Outline each blood parasite and name the species.
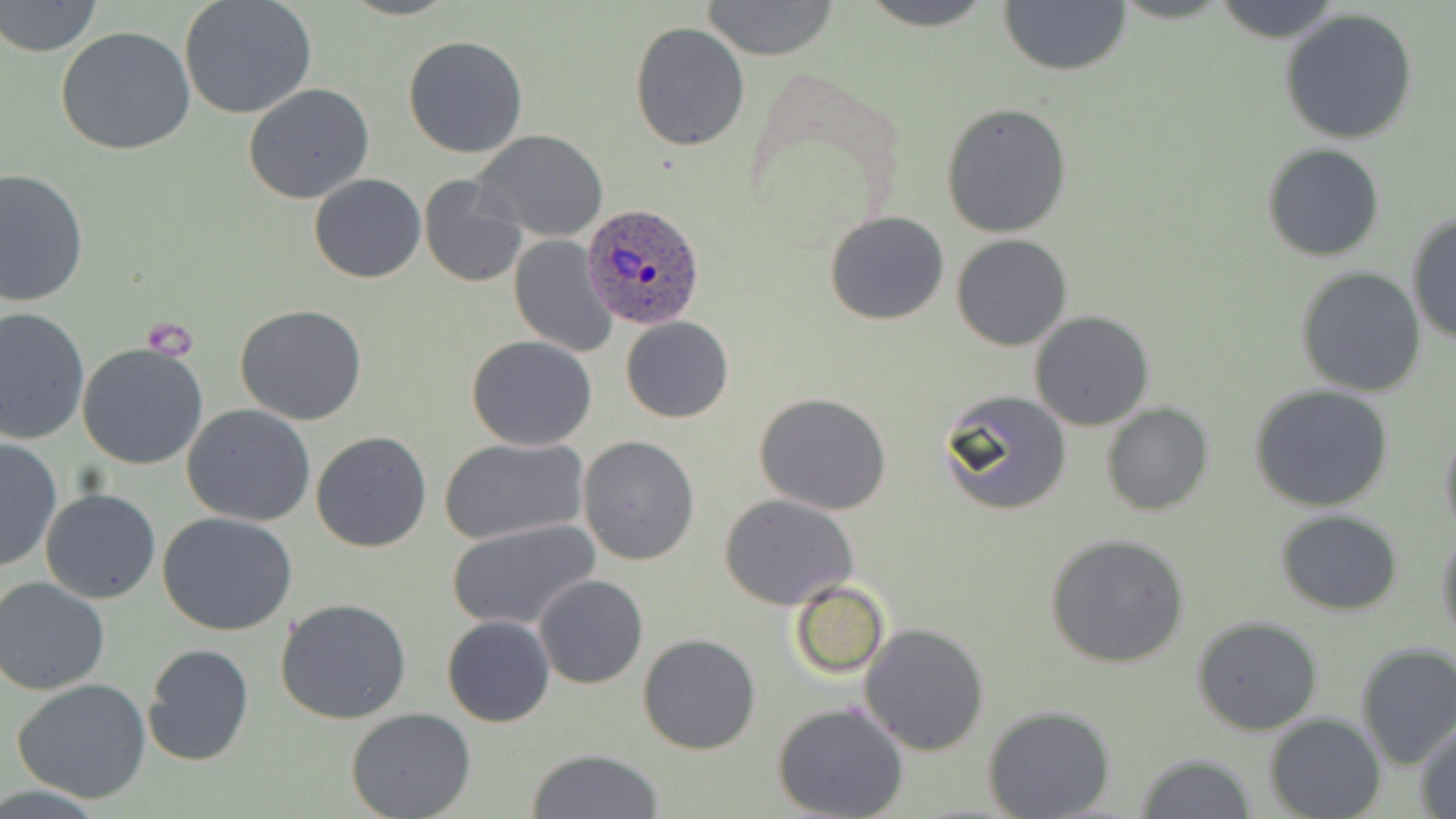
Approximate bounding boxes as (x1, y1, x2, y2) in pixels.
Plasmodium ovale-infected red blood cells: (581, 202, 705, 331).
No Plasmodium falciparum, Plasmodium malariae, Plasmodium vivax, Babesia divergens, or Trypanosoma brucei observed.

Summary:
  - Uninfected red blood cell locations: (178, 0, 317, 119), (702, 0, 840, 61), (859, 0, 996, 30), (998, 0, 1130, 77), (1210, 0, 1346, 45), (1, 1, 103, 57), (1278, 7, 1420, 145), (629, 21, 749, 151), (55, 25, 196, 156), (404, 34, 528, 157), (244, 84, 374, 205), (940, 102, 1072, 238), (472, 129, 608, 242), (1262, 143, 1384, 262), (0, 168, 89, 308), (310, 175, 426, 283), (418, 175, 527, 288), (825, 210, 948, 325), (1405, 211, 1455, 345), (951, 234, 1072, 351), (508, 235, 617, 357), (1296, 266, 1427, 397), (0, 305, 90, 445), (236, 305, 367, 425), (1028, 310, 1154, 432), (620, 316, 734, 424), (466, 335, 597, 451), (76, 342, 209, 470), (1250, 385, 1396, 513), (940, 388, 1073, 517), (755, 393, 892, 516), (1101, 402, 1214, 517), (182, 404, 315, 528), (1439, 419, 1456, 544), (310, 431, 432, 552), (437, 436, 590, 545), (578, 436, 700, 566), (0, 437, 62, 575), (40, 487, 160, 604), (719, 492, 858, 610), (1274, 509, 1403, 615), (157, 513, 299, 638), (447, 519, 600, 632), (1436, 529, 1456, 644), (1044, 532, 1191, 669), (534, 574, 649, 690), (0, 575, 113, 695), (789, 581, 889, 680), (276, 597, 412, 723), (441, 615, 555, 726), (1191, 616, 1324, 736), (861, 623, 989, 756), (638, 633, 760, 753), (143, 643, 255, 766), (1354, 643, 1456, 769), (10, 678, 155, 805), (773, 701, 910, 819), (347, 706, 476, 819), (982, 706, 1117, 819), (1264, 713, 1384, 819), (1414, 722, 1456, 816), (527, 749, 663, 819), (1134, 752, 1256, 818)
  - Slide-level diagnosis: Plasmodium ovale
  - Field of view: one of a larger specimen
  - Magnification: 1000x
  - Image size: 1456×819 pixels
  - Stain: May-Grünwald-Giemsa
  - Preparation: thin blood smear
  - Modality: light microscopy